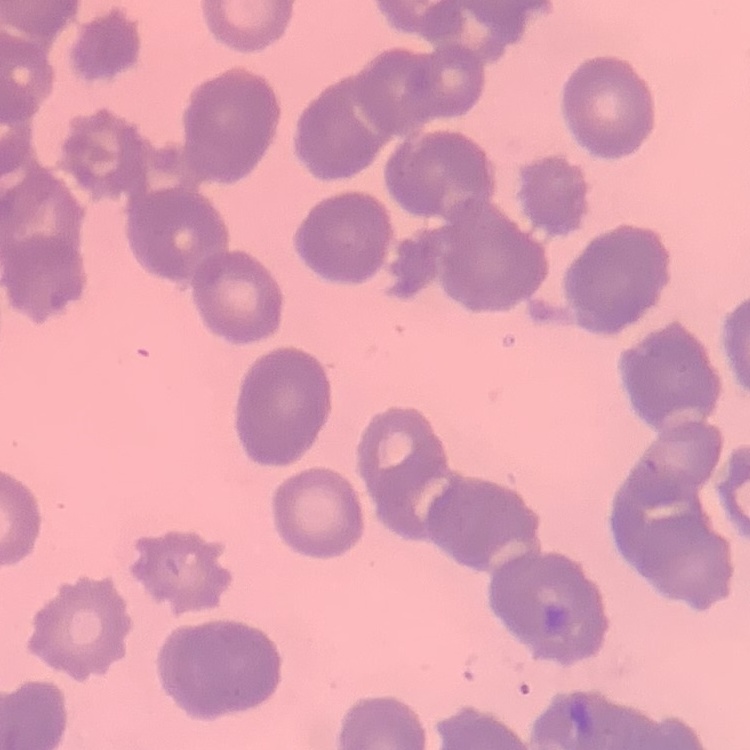

Summary:
  - Erythrocyte morphology: rouleaux formation
  - Preparation: thin blood smear
  - Image type: one tile cut from a larger photomicrograph
  - Stain: Field's or Giemsa